Comment on the morphology of the red blood cells.
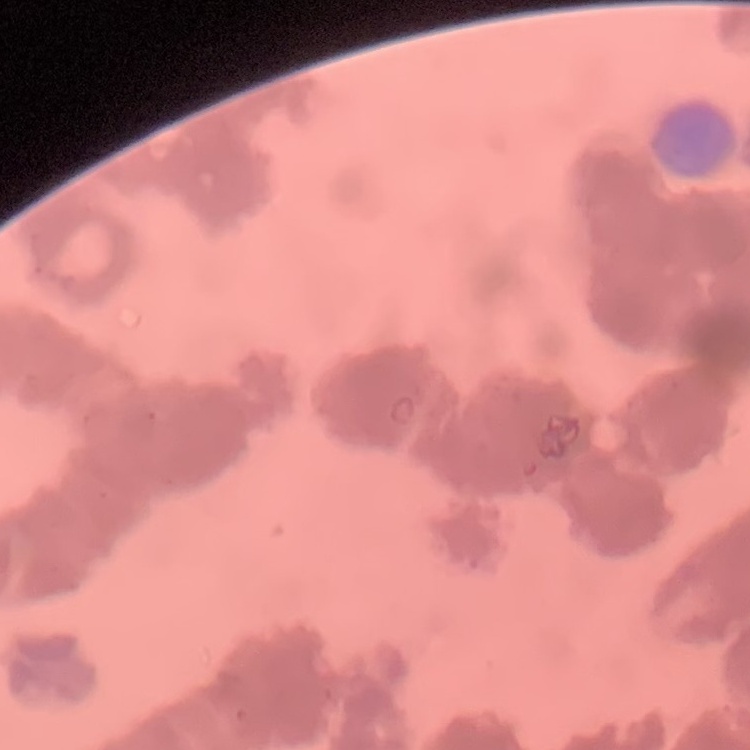

Rouleaux formation.

Stained with either Field's or Giemsa. One tile cut from a larger photomicrograph. Thin blood smear.